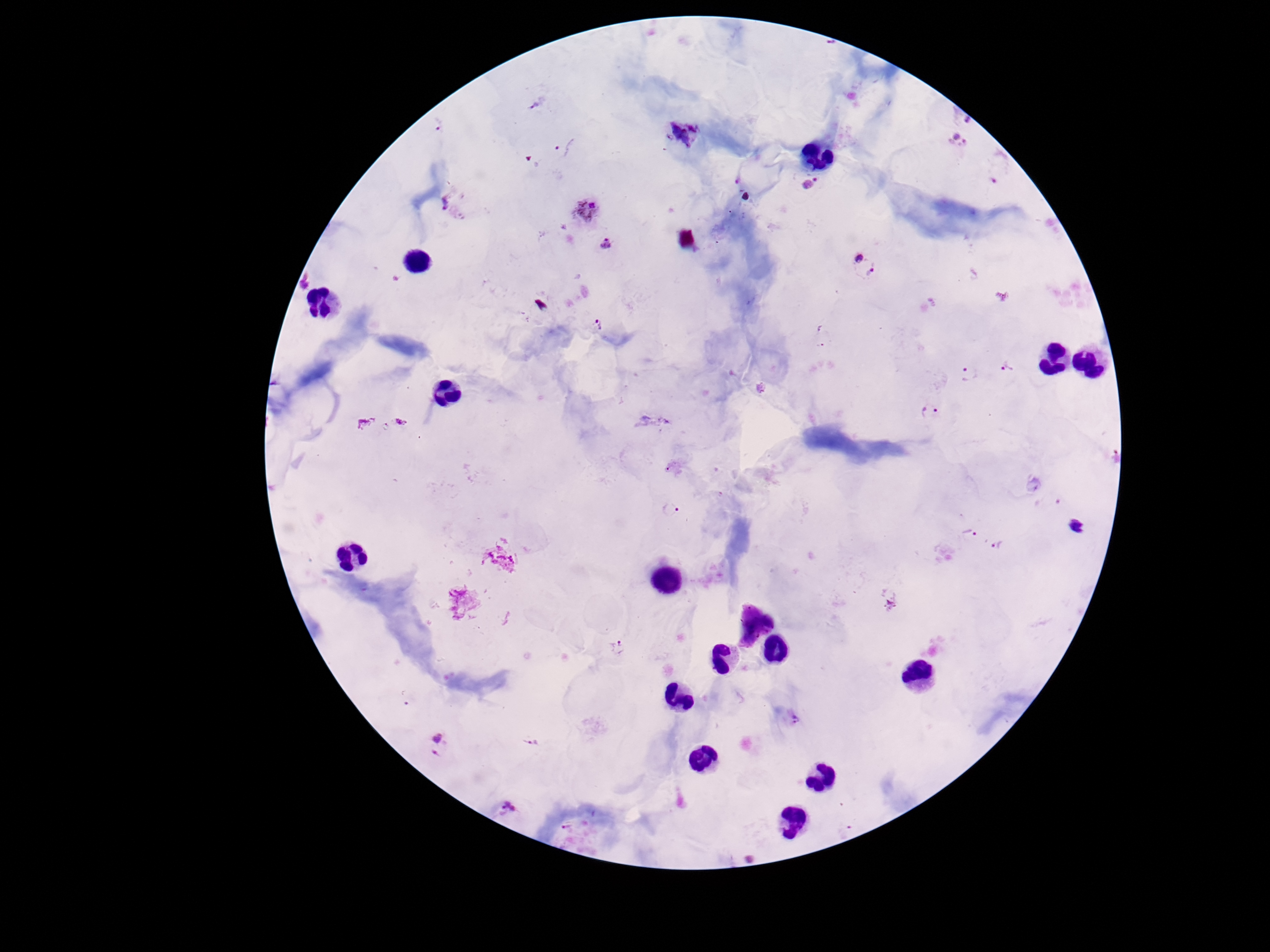 Approximate centers as {x, y} in pixels. Plasmodium parasite locations: {539, 103}, {968, 121}, {440, 126}, {683, 133}, {957, 140}, {563, 145}, {992, 180}, {810, 184}, {455, 204}, {587, 209}, {607, 244}, {858, 258}, {873, 268}, {304, 279}, {600, 325}, {821, 325}, {821, 346}, {1006, 367}, {969, 372}, {930, 413}, {382, 432}, {671, 511}, {970, 534}, {997, 547}, {890, 604}, {621, 645}, {796, 719}, {531, 742}, {437, 746}, {508, 810}, {567, 828}. Image is 1270×952 pixels. Smartphone photograph taken through the microscope eyepiece. Giemsa stain. Single field of view. Patient malaria status: positive. Thick blood smear. 100x magnification.